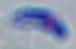
modality = micrograph
identification = Toxoplasma gondii
magnification = 1000x